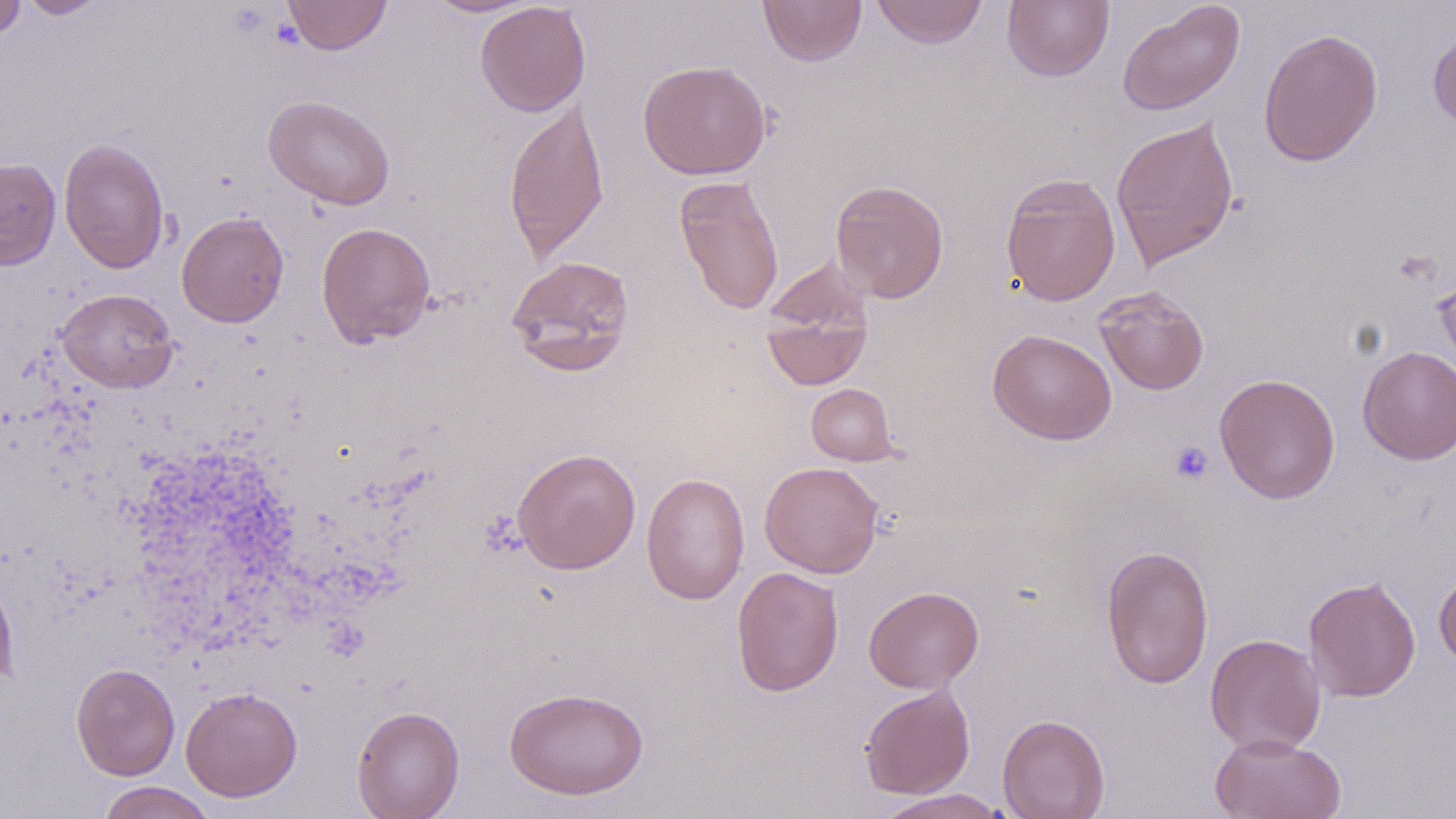

slide-level diagnosis = no evidence of blood parasites
uninfected red blood cell locations = approximate bounding boxes as named x1/y1/x2/y2 corners in pixels: (x1=0, y1=0, x2=26, y2=42), (x1=17, y1=0, x2=108, y2=18), (x1=282, y1=0, x2=392, y2=56), (x1=422, y1=0, x2=541, y2=18), (x1=757, y1=0, x2=868, y2=66), (x1=871, y1=0, x2=989, y2=49), (x1=1002, y1=0, x2=1114, y2=82), (x1=475, y1=1, x2=591, y2=117), (x1=1117, y1=1, x2=1245, y2=116), (x1=1258, y1=27, x2=1384, y2=167), (x1=1427, y1=29, x2=1456, y2=130), (x1=638, y1=60, x2=771, y2=180), (x1=263, y1=95, x2=395, y2=210), (x1=503, y1=98, x2=610, y2=264), (x1=1111, y1=116, x2=1240, y2=270), (x1=59, y1=137, x2=170, y2=274), (x1=0, y1=158, x2=60, y2=270), (x1=1000, y1=172, x2=1121, y2=307), (x1=674, y1=175, x2=784, y2=315), (x1=830, y1=179, x2=950, y2=303), (x1=177, y1=211, x2=289, y2=327), (x1=316, y1=221, x2=436, y2=348), (x1=506, y1=254, x2=635, y2=374), (x1=1433, y1=265, x2=1456, y2=378), (x1=759, y1=266, x2=875, y2=392), (x1=1094, y1=286, x2=1210, y2=395), (x1=56, y1=288, x2=179, y2=393), (x1=987, y1=328, x2=1117, y2=445), (x1=1357, y1=345, x2=1456, y2=464), (x1=1214, y1=373, x2=1341, y2=504), (x1=806, y1=383, x2=899, y2=465), (x1=512, y1=447, x2=641, y2=574), (x1=759, y1=461, x2=884, y2=578), (x1=641, y1=472, x2=750, y2=605), (x1=1101, y1=544, x2=1214, y2=688), (x1=0, y1=566, x2=18, y2=690), (x1=731, y1=566, x2=844, y2=697), (x1=1434, y1=568, x2=1456, y2=670), (x1=1303, y1=576, x2=1421, y2=702), (x1=864, y1=586, x2=984, y2=693), (x1=1204, y1=633, x2=1326, y2=756), (x1=70, y1=662, x2=180, y2=781), (x1=859, y1=684, x2=975, y2=799), (x1=504, y1=685, x2=648, y2=800), (x1=180, y1=686, x2=303, y2=802), (x1=352, y1=705, x2=465, y2=819), (x1=997, y1=714, x2=1110, y2=819), (x1=1209, y1=731, x2=1346, y2=819), (x1=95, y1=781, x2=218, y2=819), (x1=873, y1=789, x2=1011, y2=818)
image size = 1456×819 pixels
platelet locations = approximate bounding boxes as named x1/y1/x2/y2 corners in pixels: (x1=1169, y1=441, x2=1214, y2=485)
magnification = 1000x
preparation = thin blood smear
field of view = single
modality = optical microscopy
stain = May-Grünwald-Giemsa